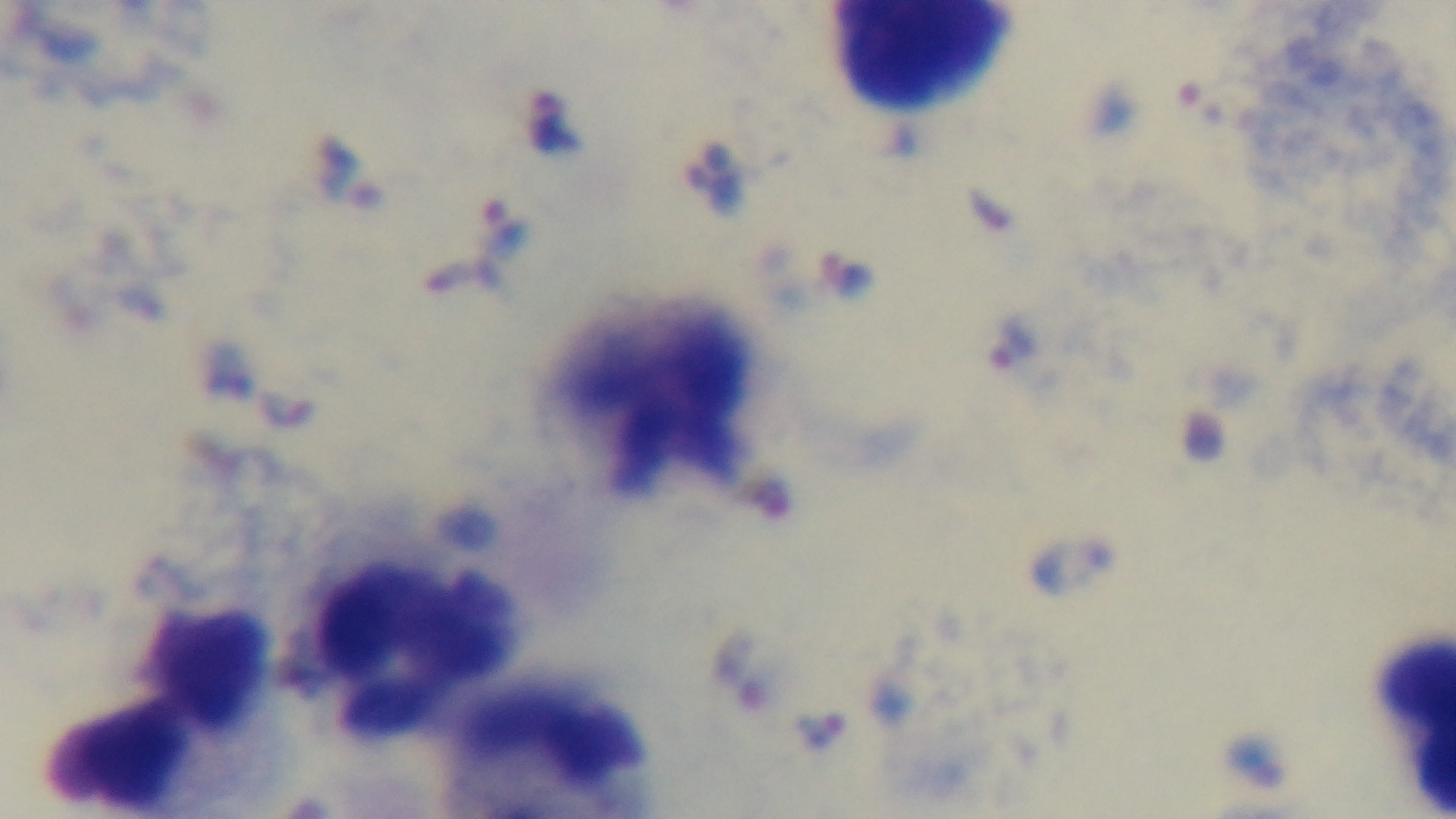
Summary:
  - Field of view: one from the slide
  - Modality: light microscopy
  - Objective: 100x oil immersion
  - Preparation: thick
  - Malaria status: infected
  - Stain: Giemsa
  - Capture: mounted 4K digital camera